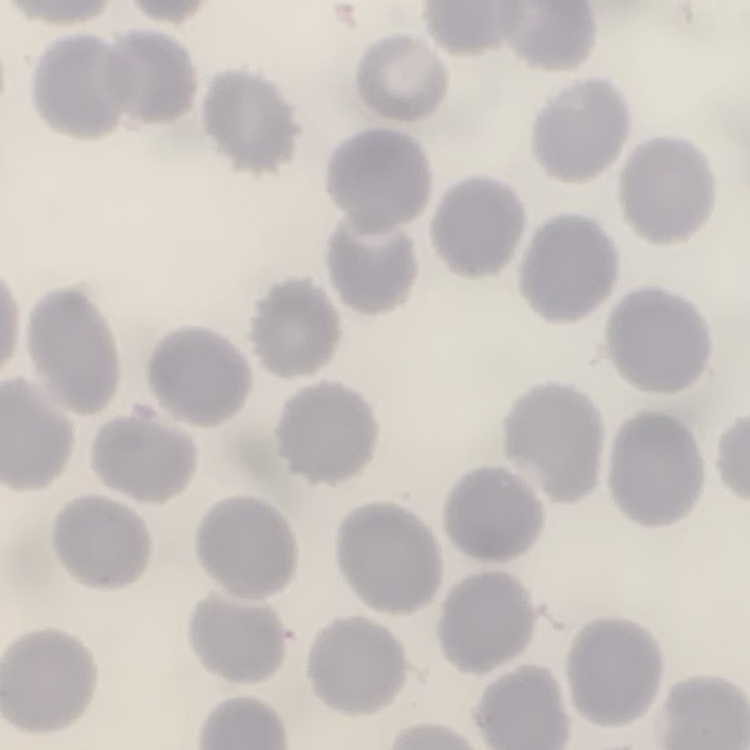
Summary:
  - Red blood cell morphology: no rouleaux formation
  - Stain: Field's or Giemsa
  - Image type: square crop of a larger photomicrograph
  - Preparation: thin blood film